Locate every leukocyte (white blood cell).
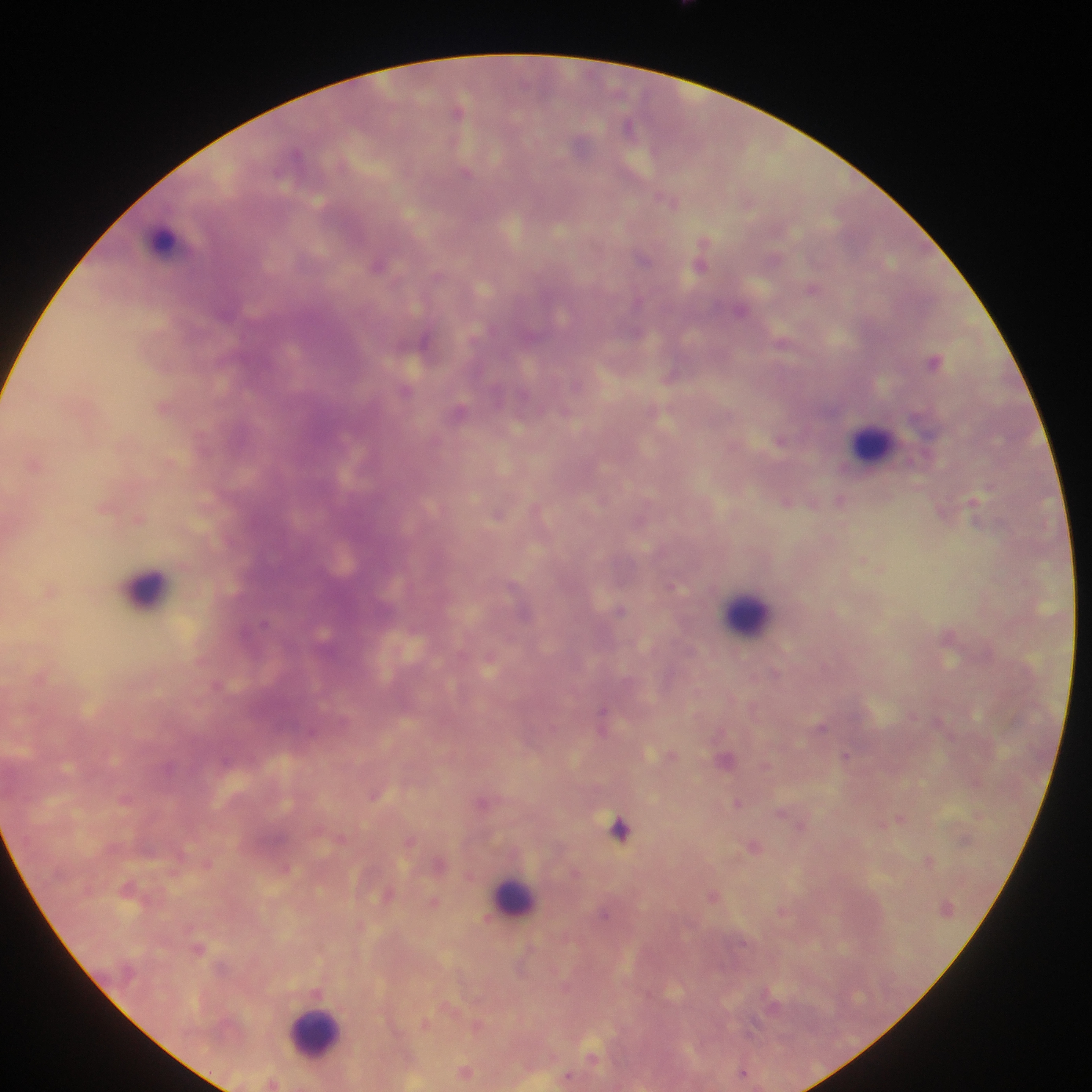
Approximate centers as {x, y} in pixels.
Leukocytes: {170, 242}, {875, 437}, {144, 585}, {744, 606}, {513, 898}, {311, 1025}.

Malaria parasite locations: {604, 710}, {847, 755}, {375, 794}, {344, 837}, {411, 841}, {593, 1055}. One field of view. Mobile-phone photograph taken through the microscope. Thick blood film. Image is 1092×1092 pixels. Collected in Ghana.